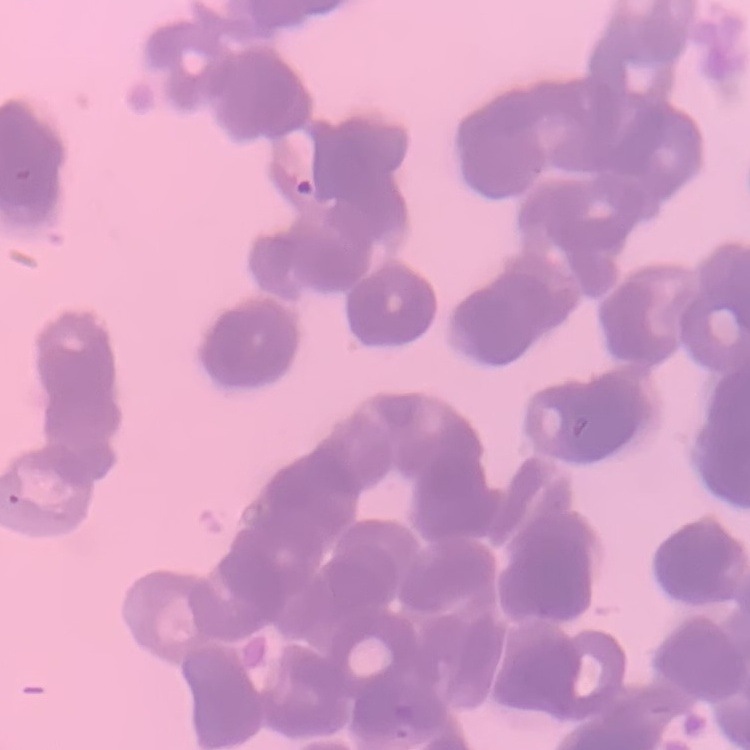

The erythrocytes exhibit rouleaux formation. Square crop of a larger photomicrograph. Stained with either Field's or Giemsa. Thin peripheral smear.